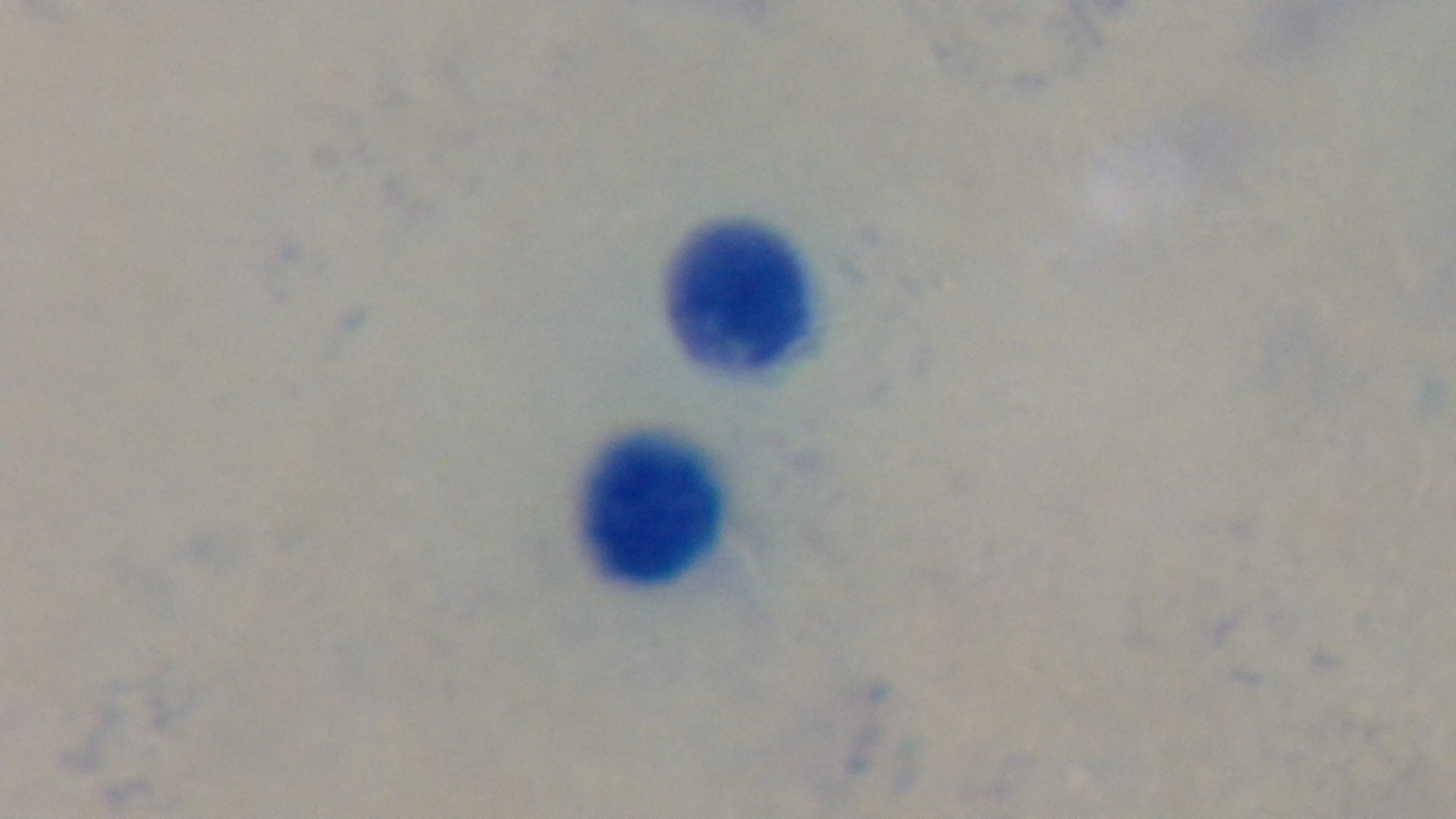
modality = light microscopy
objective = 100x oil immersion
malaria status = negative
preparation = thick blood film
capture = mounted 4K digital camera
stain = Giemsa
field of view = one from the slide